Comment on the morphology of the erythrocytes.
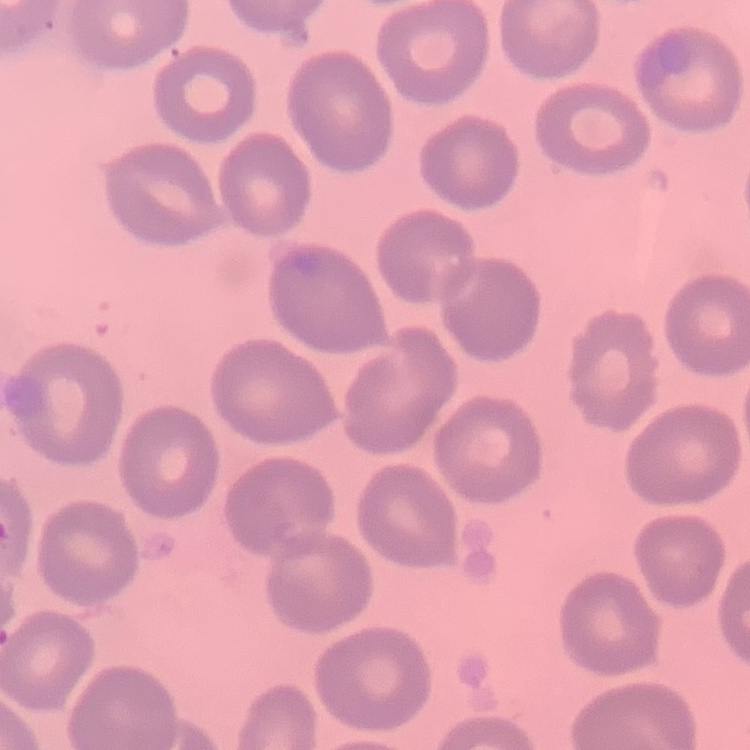

No rouleaux formation.

Summary:
  - Preparation: thin peripheral smear
  - Image type: one tile cut from a larger photomicrograph
  - Stain: Field's or Giemsa